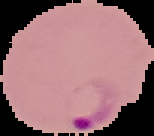
image_size: 154×136 pixels
image_type: segmented cell region on a black background
preparation: thin blood smear
result: malaria parasites detected